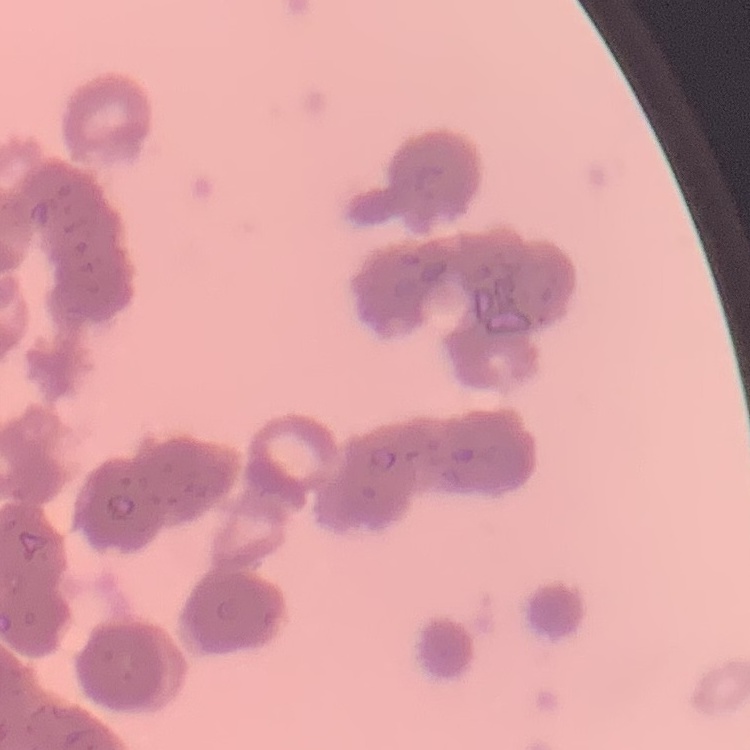

{
  "red_blood_cell_morphology": "rouleaux formation",
  "preparation": "thin blood film",
  "stain": "Field's or Giemsa",
  "image_type": "one tile cut from a larger photomicrograph"
}